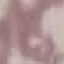

Summary:
  - Result: no malaria parasites detected
  - Stain: Giemsa
  - Image type: cell patch, automatically extracted from a larger field of view and resized to 64 × 64 pixels
  - Capture: smartphone through the microscope eyepiece
  - Preparation: thin blood smear